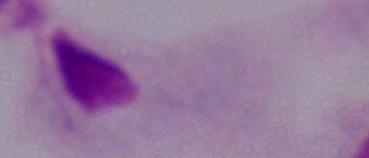

magnification = 1000x
identification = trichomonad
modality = photomicrograph